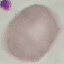
Result: no malaria parasites detected. Acquired by smartphone through the microscope eyepiece. Thin blood film. Giemsa stain. Automatically extracted cell patch, resized to 64 × 64 pixels.